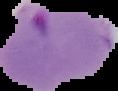

Image is 118×91 pixels. Malaria status: parasitized. Segmented cell region on a black background. From a thin blood smear.